Locate every Plasmodium vivax-infected red blood cell.
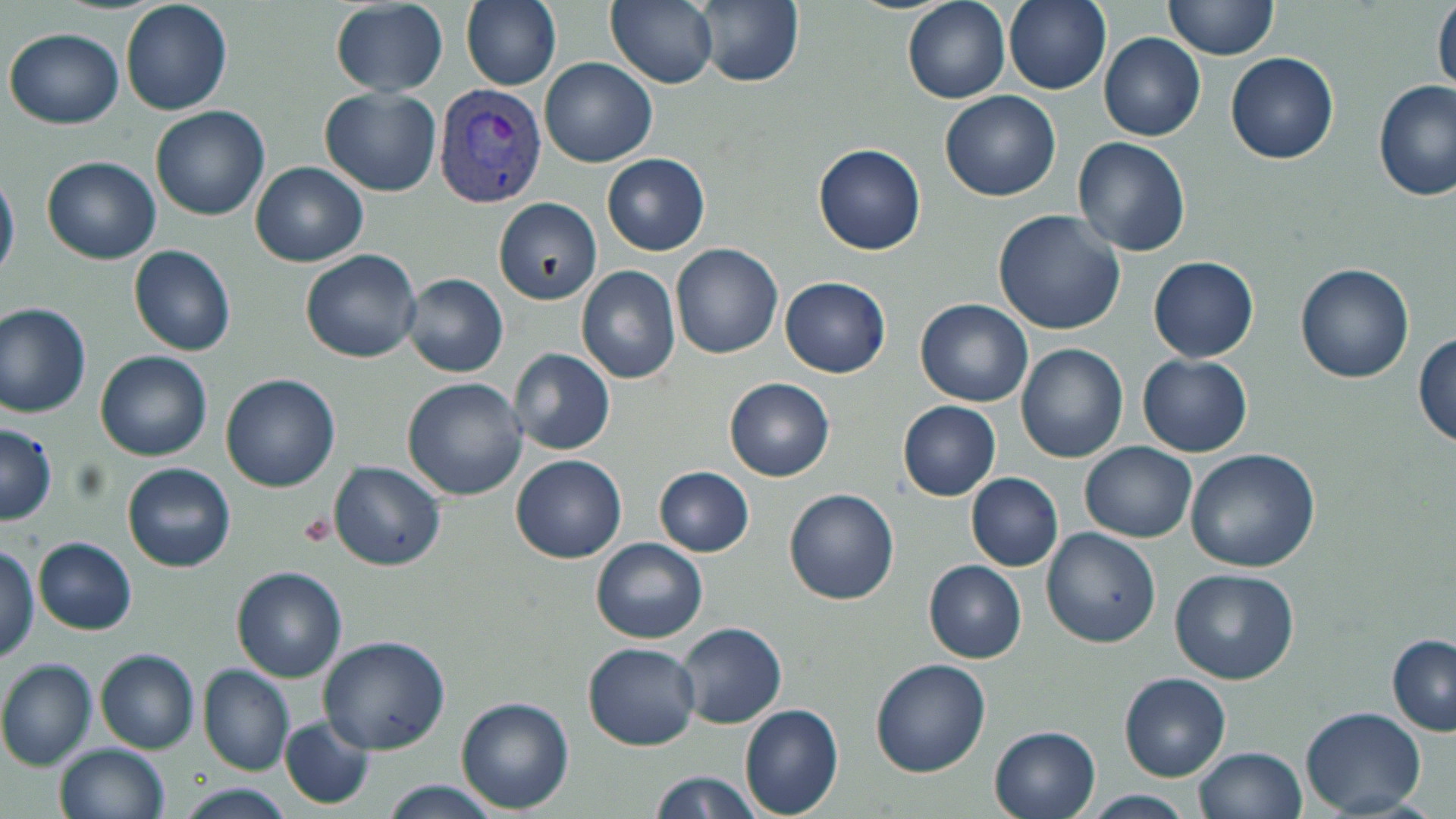
Approximate bounding boxes as (x1, y1, x2, y2) in pixels.
Plasmodium vivax-infected red blood cells: (433, 82, 550, 207).

Uninfected red blood cell locations: (121, 0, 233, 114), (459, 0, 564, 91), (606, 0, 719, 89), (696, 0, 803, 88), (902, 0, 1009, 103), (1001, 0, 1112, 96), (1163, 0, 1279, 60), (1432, 0, 1456, 99), (331, 1, 448, 95), (5, 28, 125, 129), (1100, 33, 1205, 141), (1226, 52, 1339, 164), (540, 57, 657, 167), (1373, 79, 1455, 202), (320, 87, 442, 196), (940, 90, 1059, 202), (151, 106, 269, 220), (1072, 138, 1192, 256), (814, 142, 927, 255), (602, 152, 711, 255), (43, 156, 161, 265), (251, 162, 368, 266), (0, 169, 19, 284), (495, 198, 601, 305), (993, 210, 1127, 335), (672, 242, 784, 358), (128, 245, 238, 355), (300, 248, 424, 363), (1148, 256, 1259, 362), (575, 258, 788, 370), (1295, 263, 1414, 383), (577, 265, 682, 384), (402, 272, 508, 378), (779, 275, 891, 378), (916, 297, 1034, 406), (0, 301, 94, 417), (1413, 331, 1455, 447), (1016, 343, 1128, 463), (508, 347, 616, 455), (96, 350, 212, 460), (1137, 353, 1253, 457), (222, 374, 342, 492), (401, 377, 526, 499), (725, 377, 835, 481), (897, 400, 1001, 501), (0, 423, 57, 525), (1080, 442, 1196, 540), (1184, 447, 1319, 573), (511, 454, 627, 563), (122, 462, 237, 573), (329, 462, 446, 571), (654, 466, 755, 556), (966, 473, 1063, 571), (784, 488, 900, 605), (1042, 525, 1161, 646), (591, 537, 708, 643), (34, 538, 137, 634), (0, 544, 40, 664), (924, 560, 1026, 663), (232, 567, 348, 682), (1168, 568, 1299, 683), (675, 621, 787, 729), (319, 636, 451, 754), (1387, 636, 1455, 736), (583, 642, 701, 749), (97, 649, 201, 752), (0, 658, 97, 769), (871, 658, 990, 776), (199, 664, 295, 775), (1119, 672, 1231, 780), (456, 697, 575, 813), (739, 704, 845, 817), (1302, 706, 1426, 814), (280, 716, 375, 809), (989, 726, 1102, 819), (56, 744, 168, 819), (1193, 747, 1306, 819), (646, 769, 764, 819), (381, 780, 504, 819), (172, 783, 296, 819), (1082, 791, 1198, 819). Slide-level diagnosis: Plasmodium vivax. Image is 1456×819 pixels. Optical microscopy. One field of a larger specimen. May-Grünwald-Giemsa stain. Captured at 1000x magnification. Thin blood smear.